Identify the cell.
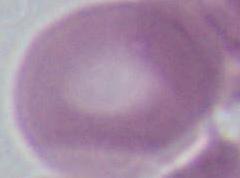
This is an erythrocyte.

1000x magnification. Photomicrograph.